Identify the cell.
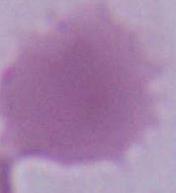

An erythrocyte.

Summary:
  - Modality: micrograph
  - Magnification: 1000x